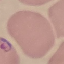
Summary:
  - Result: malaria parasites identified
  - Image type: automatically extracted cell patch, resized to 64 × 64 pixels
  - Capture: smartphone camera at the microscope eyepiece
  - Preparation: thin blood film
  - Stain: Giemsa